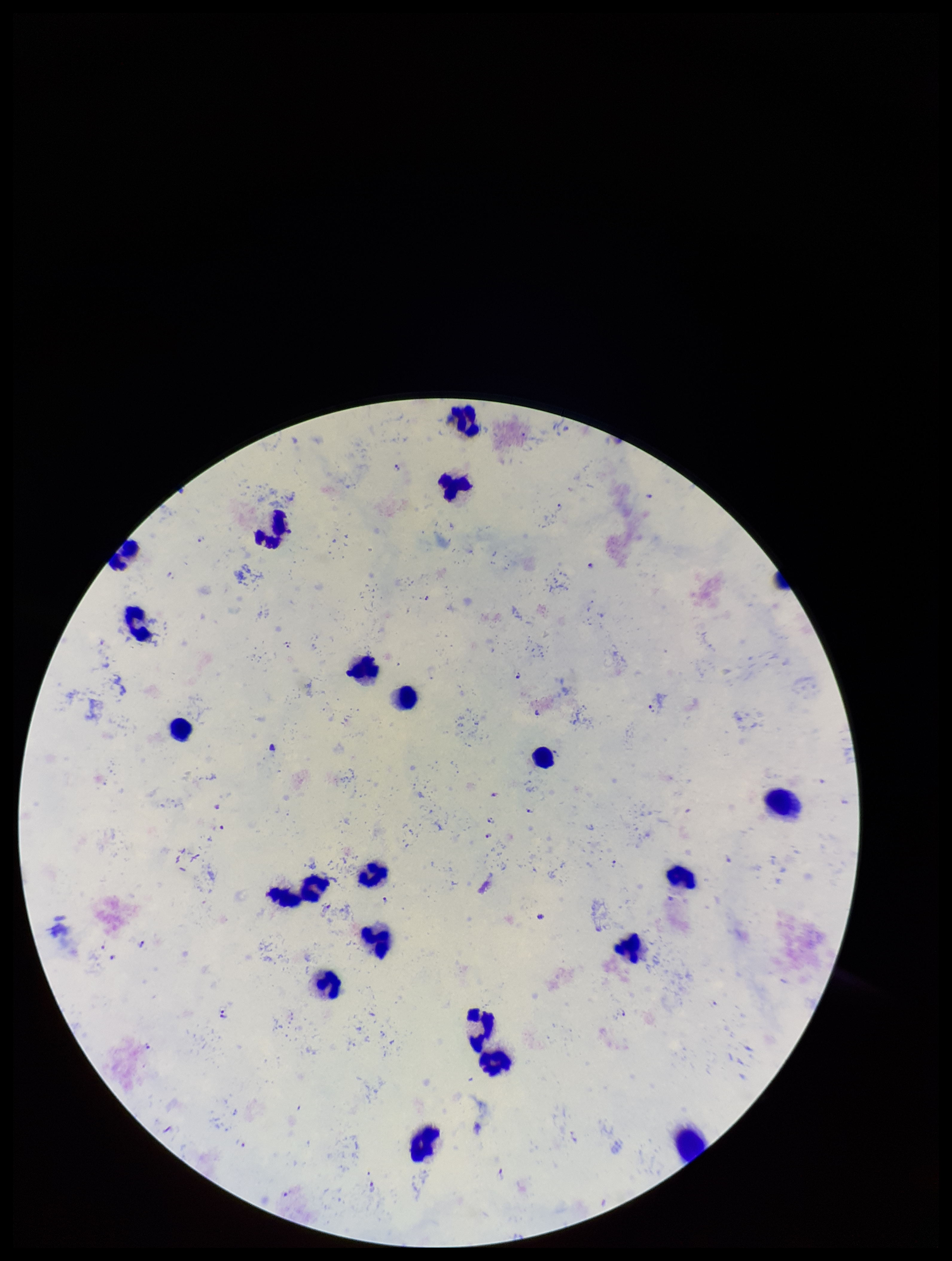
species reported for this patient = Plasmodium falciparum
capture = smartphone photograph through the microscope eyepiece
field of view = single
image size = 952×1261 pixels
parasite count = 26
stain = Giemsa
Plasmodium parasites = identified
leukocyte count = 20
preparation = thick smear
patient malaria status = infected